Identify the cell.
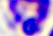
A leukocyte.

Summary:
  - Modality: micrograph
  - Magnification: 400x